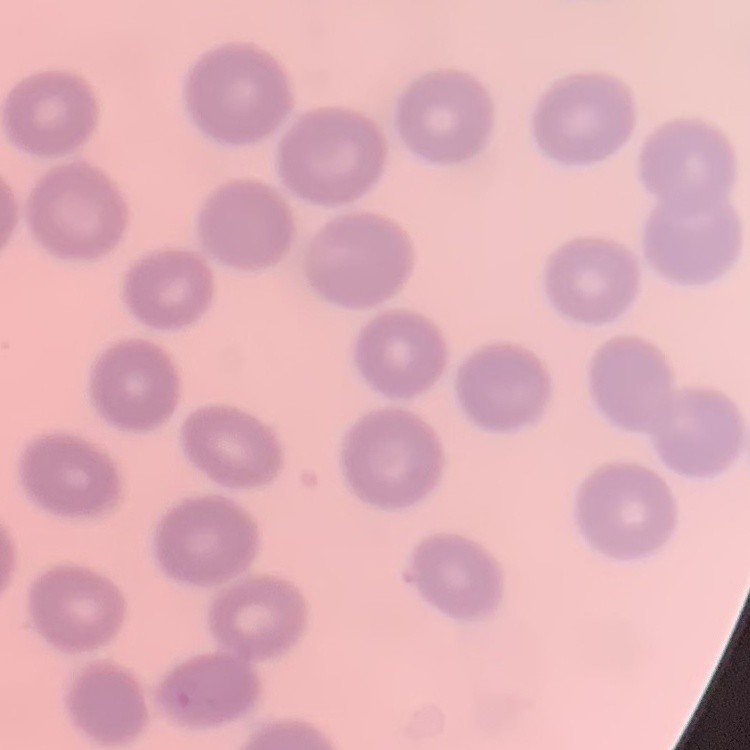
{
  "erythrocyte_morphology": "no rouleaux formation",
  "preparation": "thin blood smear",
  "stain": "Field's or Giemsa",
  "image_type": "square crop of a larger photomicrograph"
}